Identify the parasite.
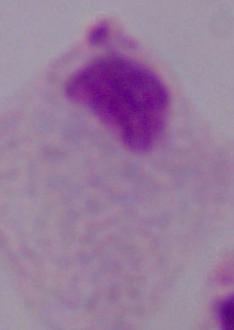

A trichomonad.

Photomicrograph. Captured at 1000x magnification.